Locate Plasmodium parasites and leukocytes.
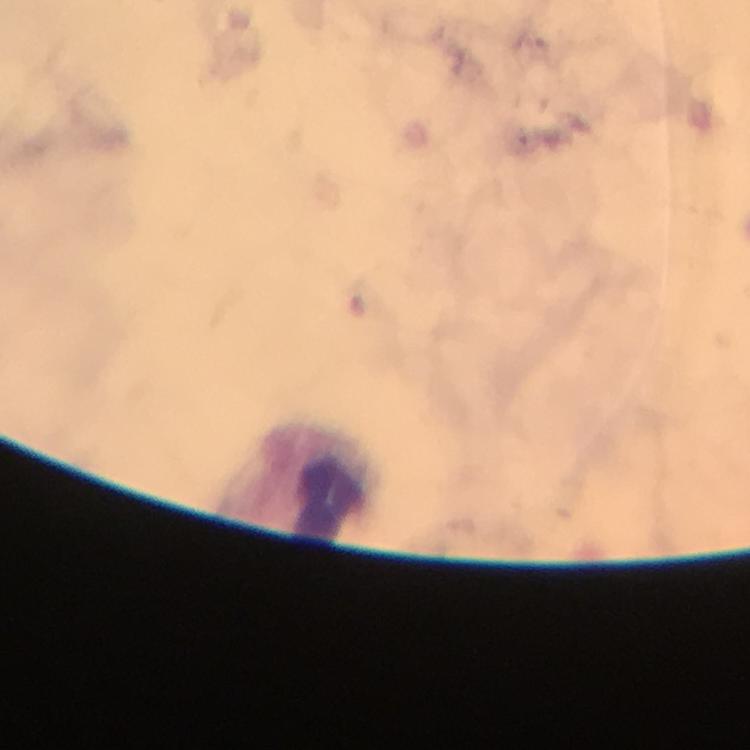

No Plasmodium parasites detected.
Approximate centers as {x, y} in pixels.
Leukocytes: {322, 488}.

Image is 750×750 pixels. Giemsa stain. Photographed through the microscope with a smartphone camera. Cropped region of a single field of view. 100x magnification. Thick smear. From a malaria diagnostic workup. Immersion oil was used.